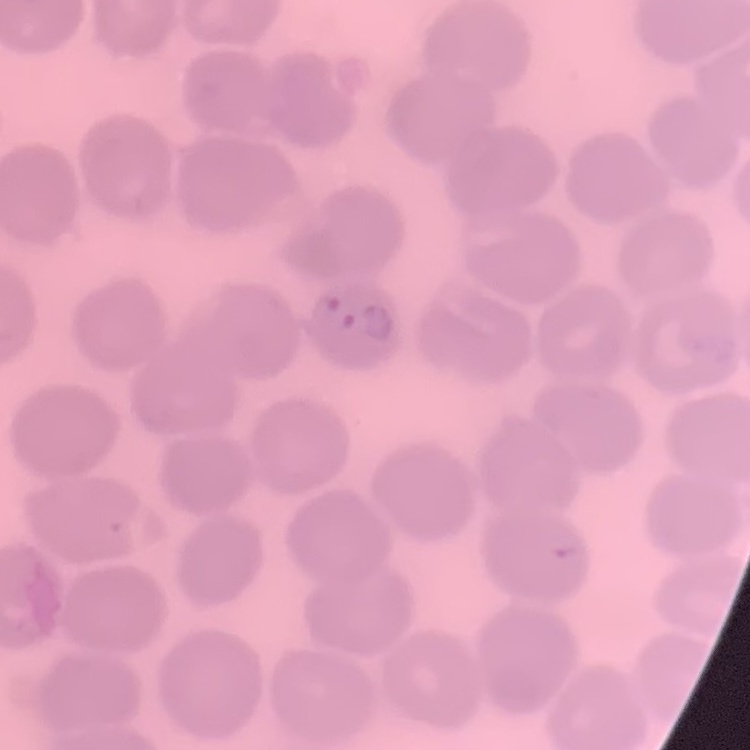

Summary:
  - Red blood cell morphology: no rouleaux formation
  - Preparation: thin peripheral smear
  - Image type: square crop of a larger photomicrograph
  - Stain: Field's or Giemsa